Assess the morphology of the red blood cells.
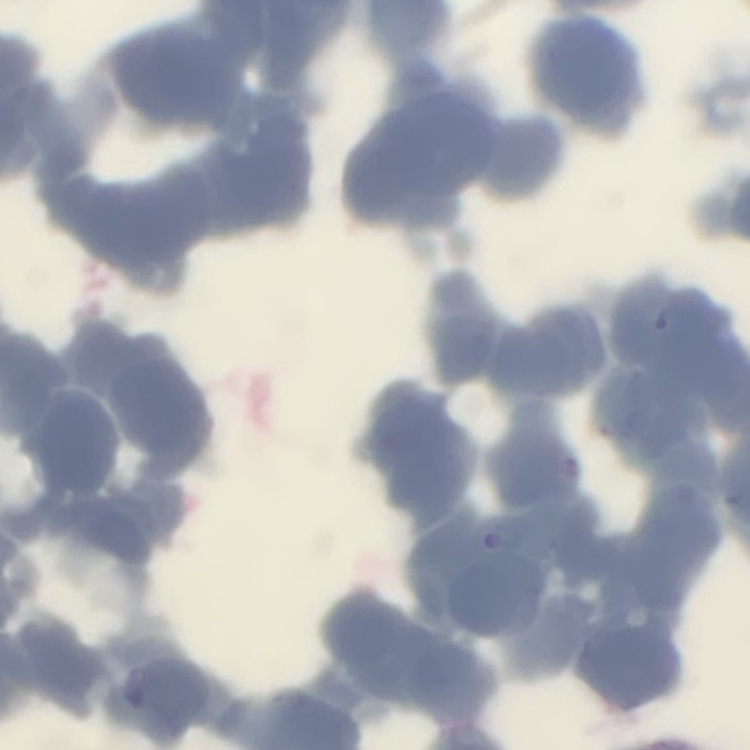

Rouleaux formation.

Thin blood film. One tile cut from a larger photomicrograph. Field's or Giemsa stain.